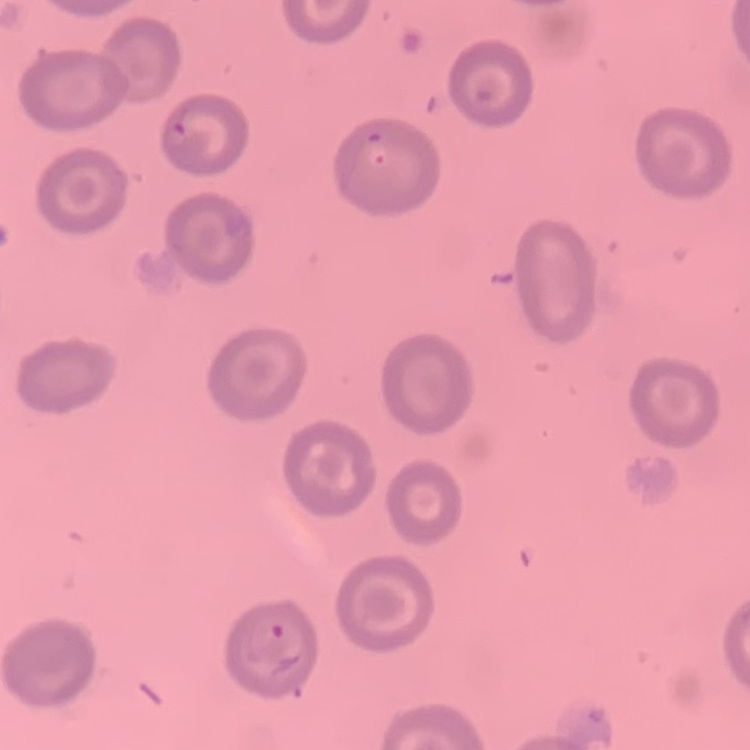

red blood cell morphology = no rouleaux formation
image type = one tile cut from a larger photomicrograph
preparation = thin blood film
stain = Field's or Giemsa